Locate every P. falciparum parasite and identify its life-cycle stage.
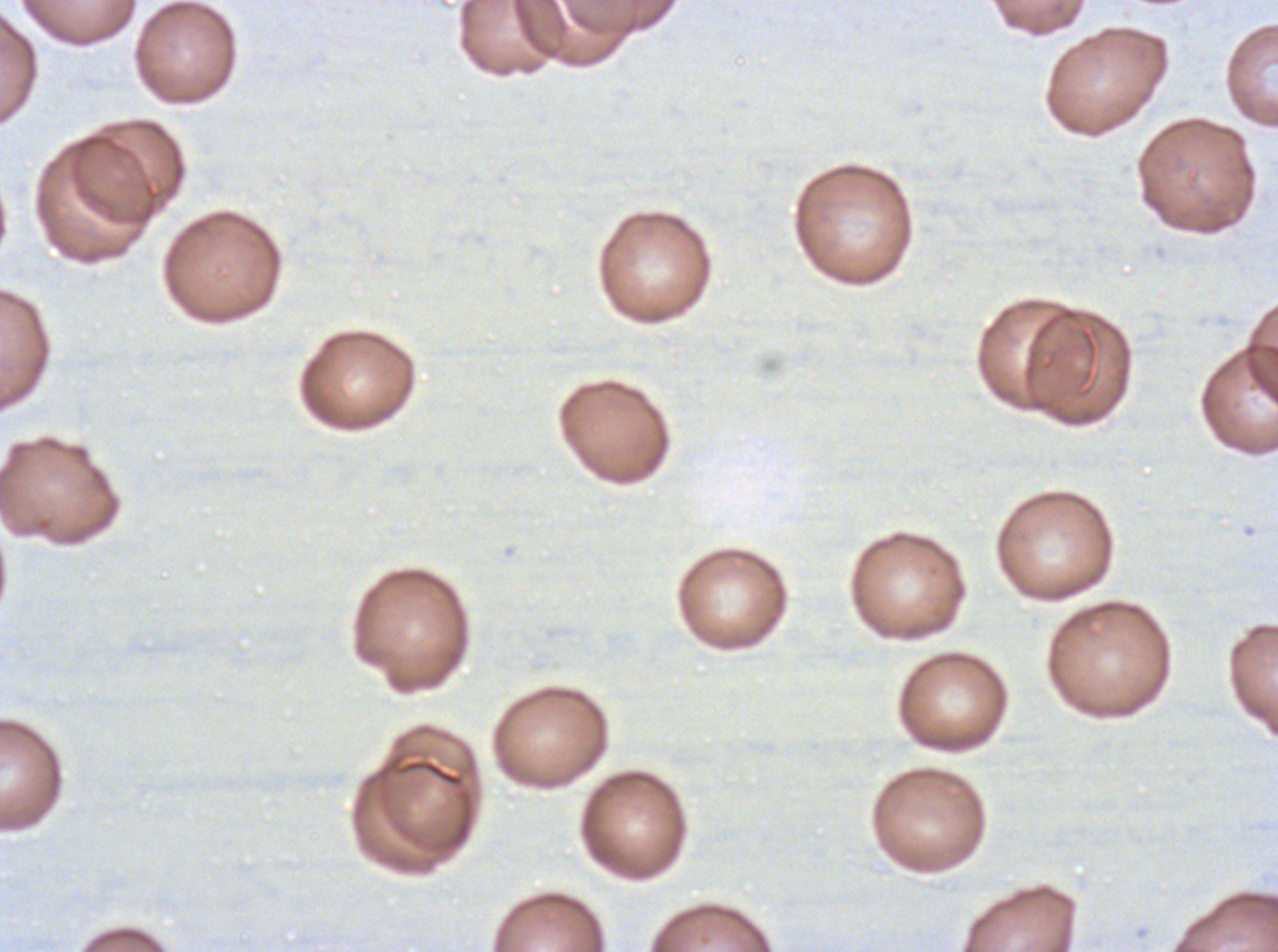

No rings, late-ring/early-trophozoite forms, mid trophozoites, late trophozoites, early schizonts, late schizonts, segmenters, or gametocytes observed.

Approximate bounding boxes as {x1, y1, x2, y2} in pixels.
Summary:
  - Debris locations: {398, 758, 464, 787}
  - Image size: 1278×952 pixels
  - Preparation: thin blood film
  - Stain: Giemsa
  - Field of view: one sub-image of a larger composite
  - Specimen: ex-vivo P. falciparum culture from a patient in The Gambia, grown for 24 to 48 hours